Mark where platelets are.
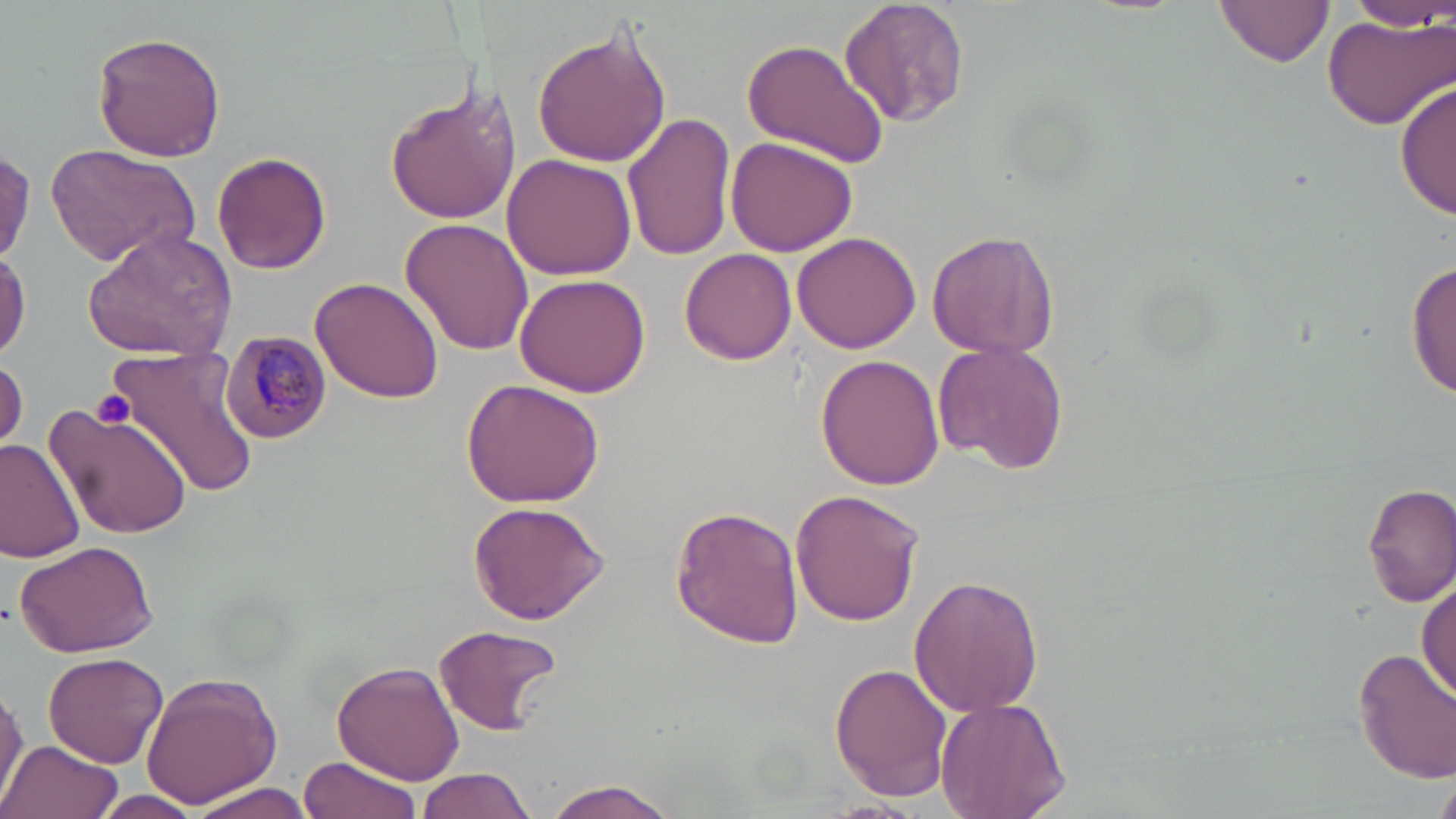
Approximate bounding boxes as (x1,y1)-(x2,y2) corner pairs in pixels.
Platelets: (93,391)-(136,430).

Summary:
  - Uninfected red blood cell locations: (838,0)-(970,130), (1216,0)-(1333,69), (1339,2)-(1450,32), (1321,9)-(1456,132), (532,25)-(672,169), (92,30)-(227,162), (741,37)-(890,169), (1397,78)-(1455,224), (385,79)-(517,227), (623,114)-(737,260), (725,136)-(860,259), (44,143)-(200,265), (0,148)-(37,262), (212,151)-(332,275), (503,154)-(639,281), (400,219)-(534,357), (923,226)-(1061,360), (81,229)-(238,360), (795,233)-(922,355), (0,245)-(29,361), (679,249)-(797,365), (1406,257)-(1455,401), (513,274)-(651,398), (309,277)-(445,403), (932,338)-(1070,474), (107,344)-(262,501), (817,354)-(945,489), (1,357)-(27,451), (460,378)-(606,507), (45,399)-(194,543), (0,439)-(86,563), (1363,482)-(1456,607), (790,490)-(924,626), (467,499)-(609,625), (669,505)-(806,650), (14,537)-(157,657), (908,573)-(1045,717), (1416,575)-(1454,704), (431,623)-(566,735), (1354,647)-(1456,782), (42,652)-(168,769), (332,661)-(465,784), (830,663)-(953,802), (139,671)-(283,808), (0,680)-(27,814), (935,696)-(1072,819), (4,737)-(122,819), (299,755)-(424,819), (414,768)-(537,819), (1436,778)-(1456,819), (541,779)-(679,819), (183,780)-(320,819), (94,791)-(202,819)
  - Plasmodium malariae-infected red blood cell locations: (220,332)-(331,441)
  - Slide-level diagnosis: Plasmodium malariae
  - Image size: 1456×819 pixels
  - Magnification: 1000x
  - Preparation: thin blood film
  - Modality: optical microscopy
  - Stain: May-Grünwald-Giemsa
  - Field of view: single